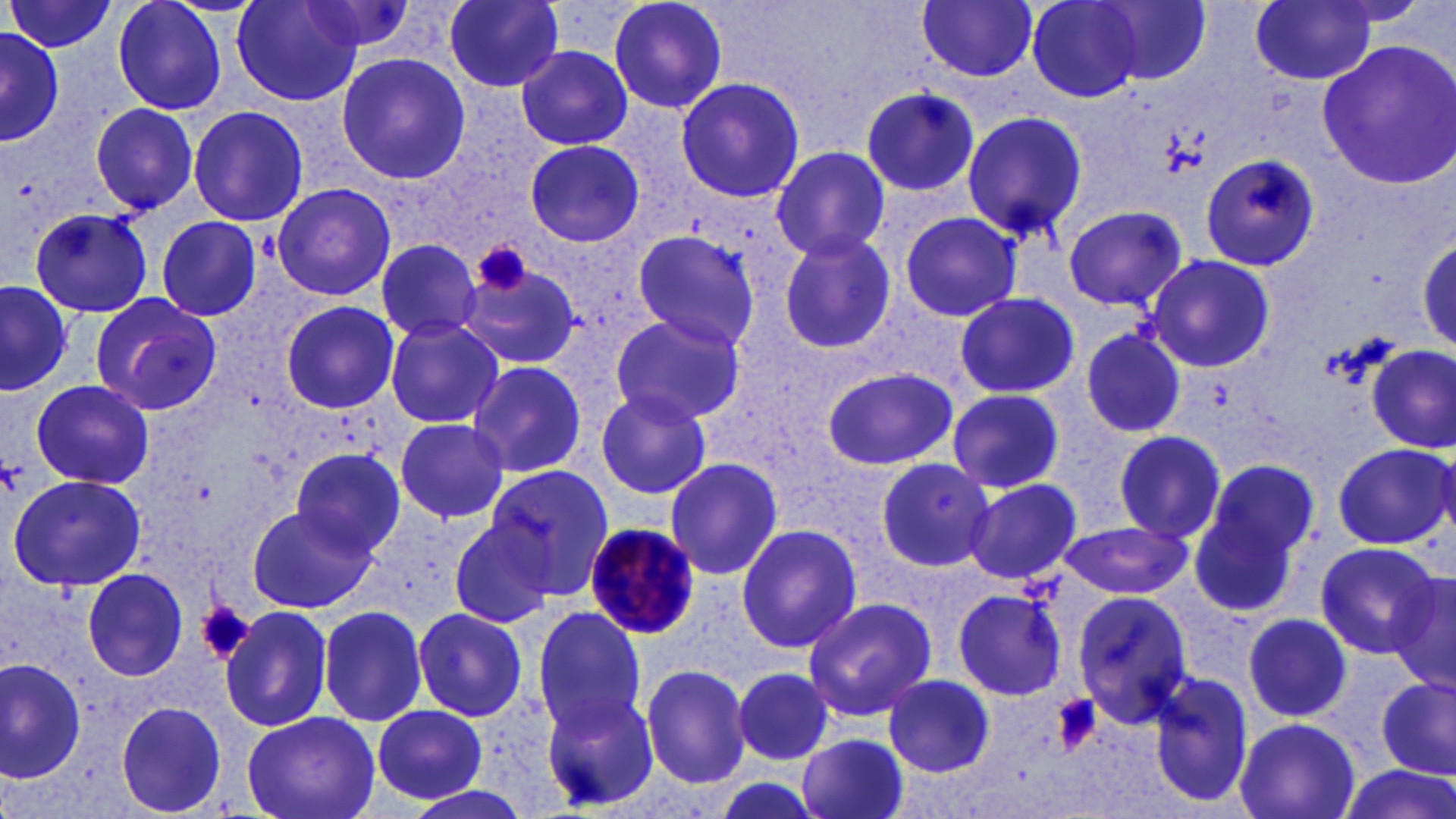

Summary:
  - Coordinate format: approximate bounding boxes as named x1/y1/x2/y2 corners in pixels
  - Platelet locations: (x1=475, y1=241, x2=533, y2=299), (x1=1, y1=461, x2=21, y2=495), (x1=198, y1=601, x2=254, y2=664), (x1=1047, y1=692, x2=1103, y2=756)
  - Plasmodium malariae-infected red blood cell locations: (x1=583, y1=522, x2=701, y2=643)
  - Uninfected red blood cell locations: (x1=111, y1=0, x2=229, y2=116), (x1=231, y1=0, x2=365, y2=107), (x1=443, y1=0, x2=565, y2=91), (x1=606, y1=0, x2=730, y2=114), (x1=918, y1=0, x2=1039, y2=82), (x1=1026, y1=0, x2=1144, y2=102), (x1=1252, y1=0, x2=1379, y2=85), (x1=5, y1=1, x2=117, y2=55), (x1=300, y1=1, x2=421, y2=58), (x1=1095, y1=2, x2=1212, y2=85), (x1=0, y1=25, x2=65, y2=147), (x1=0, y1=31, x2=65, y2=145), (x1=1317, y1=42, x2=1456, y2=189), (x1=516, y1=45, x2=633, y2=150), (x1=335, y1=52, x2=470, y2=186), (x1=673, y1=76, x2=805, y2=203), (x1=859, y1=85, x2=979, y2=199), (x1=88, y1=103, x2=200, y2=214), (x1=187, y1=105, x2=309, y2=228), (x1=961, y1=110, x2=1088, y2=243), (x1=525, y1=139, x2=646, y2=248), (x1=770, y1=146, x2=891, y2=263), (x1=1199, y1=153, x2=1321, y2=273), (x1=270, y1=182, x2=397, y2=302), (x1=1062, y1=203, x2=1187, y2=310), (x1=28, y1=208, x2=153, y2=318), (x1=898, y1=211, x2=1022, y2=319), (x1=155, y1=216, x2=263, y2=320), (x1=631, y1=229, x2=764, y2=351), (x1=776, y1=231, x2=898, y2=353), (x1=1416, y1=235, x2=1455, y2=352), (x1=374, y1=238, x2=483, y2=343), (x1=1148, y1=255, x2=1275, y2=369), (x1=460, y1=260, x2=582, y2=367), (x1=0, y1=280, x2=71, y2=395), (x1=953, y1=291, x2=1081, y2=400), (x1=87, y1=293, x2=222, y2=416), (x1=278, y1=301, x2=400, y2=414), (x1=608, y1=311, x2=746, y2=424), (x1=383, y1=318, x2=505, y2=428), (x1=1079, y1=326, x2=1189, y2=441), (x1=1368, y1=344, x2=1454, y2=453), (x1=467, y1=359, x2=587, y2=479), (x1=821, y1=367, x2=957, y2=471), (x1=31, y1=379, x2=153, y2=491), (x1=591, y1=388, x2=713, y2=499), (x1=947, y1=388, x2=1065, y2=492), (x1=394, y1=418, x2=510, y2=522), (x1=1111, y1=427, x2=1230, y2=545), (x1=1332, y1=442, x2=1454, y2=550), (x1=290, y1=447, x2=404, y2=560), (x1=662, y1=457, x2=782, y2=579), (x1=874, y1=457, x2=993, y2=571), (x1=876, y1=459, x2=998, y2=570), (x1=1192, y1=463, x2=1314, y2=612), (x1=484, y1=466, x2=616, y2=596), (x1=8, y1=474, x2=148, y2=591), (x1=962, y1=477, x2=1084, y2=586), (x1=247, y1=505, x2=371, y2=614), (x1=446, y1=517, x2=558, y2=629), (x1=1059, y1=519, x2=1191, y2=600), (x1=733, y1=523, x2=862, y2=652), (x1=1312, y1=540, x2=1442, y2=659), (x1=1384, y1=567, x2=1456, y2=696), (x1=80, y1=568, x2=188, y2=681), (x1=950, y1=586, x2=1067, y2=702), (x1=1072, y1=592, x2=1196, y2=722), (x1=799, y1=595, x2=938, y2=720), (x1=317, y1=603, x2=429, y2=726), (x1=221, y1=606, x2=333, y2=732), (x1=530, y1=607, x2=649, y2=735), (x1=410, y1=608, x2=528, y2=722), (x1=1243, y1=612, x2=1352, y2=721), (x1=1, y1=658, x2=87, y2=783), (x1=640, y1=663, x2=753, y2=789), (x1=733, y1=668, x2=834, y2=767), (x1=1148, y1=671, x2=1255, y2=808), (x1=884, y1=673, x2=995, y2=775), (x1=1376, y1=676, x2=1455, y2=778), (x1=542, y1=687, x2=660, y2=808), (x1=115, y1=702, x2=226, y2=816), (x1=372, y1=704, x2=488, y2=804), (x1=242, y1=711, x2=379, y2=819), (x1=1234, y1=715, x2=1362, y2=819), (x1=797, y1=733, x2=912, y2=819), (x1=1340, y1=763, x2=1455, y2=819), (x1=703, y1=774, x2=831, y2=819), (x1=398, y1=782, x2=538, y2=819)
  - Slide-level diagnosis: Plasmodium malariae
  - Field of view: one of a larger specimen
  - Modality: optical microscopy
  - Image size: 1456×819 pixels
  - Magnification: 1000x
  - Stain: May-Grünwald-Giemsa
  - Preparation: thin blood smear